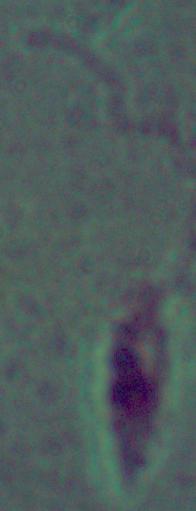

modality = micrograph
magnification = 1000x
identification = Leishmania